Locate every blood parasite and identify its species.
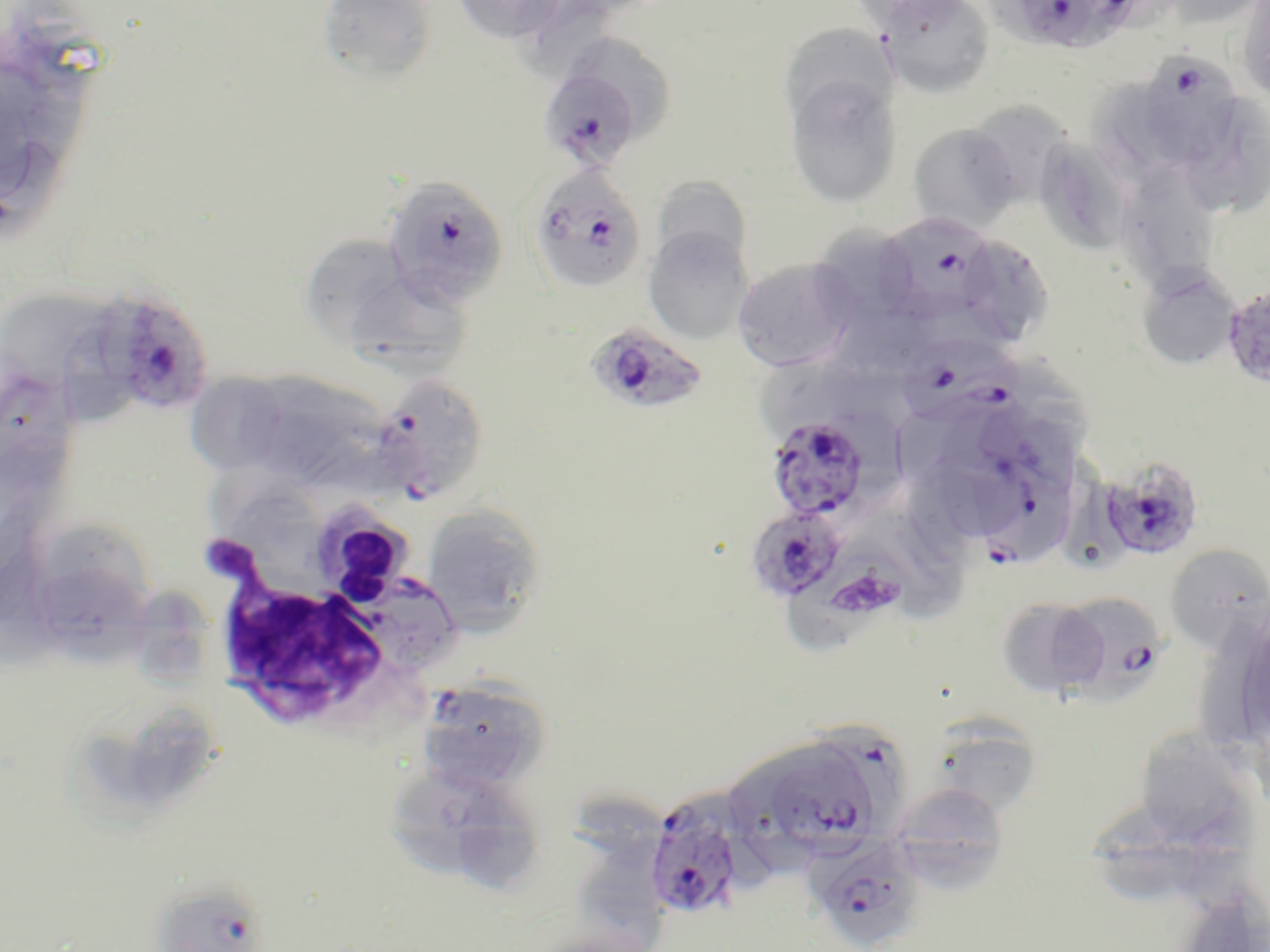
Approximate bounding boxes as (x1, y1, x2, y2) in pixels.
Plasmodium falciparum-infected red blood cells: (991, 0, 1149, 56), (1145, 53, 1235, 159), (547, 73, 633, 172), (528, 166, 647, 295), (382, 175, 507, 310), (880, 216, 995, 324), (91, 291, 214, 415), (585, 321, 710, 415), (905, 339, 1032, 430), (368, 374, 490, 503), (764, 415, 876, 522), (972, 450, 1075, 573), (1102, 455, 1205, 562), (745, 505, 847, 603), (1059, 595, 1166, 704), (417, 675, 553, 793), (817, 724, 911, 825), (775, 758, 875, 857), (644, 797, 743, 921), (807, 831, 927, 951), (151, 879, 271, 952).
No Plasmodium ovale, Plasmodium malariae, Plasmodium vivax, Babesia divergens, or Trypanosoma brucei observed.

Summary:
  - Platelet locations: (838, 577, 907, 618)
  - White blood cell locations: (215, 513, 398, 730)
  - Uninfected red blood cell locations: (317, 0, 438, 84), (451, 0, 574, 44), (849, 0, 974, 31), (1150, 0, 1268, 29), (1235, 0, 1270, 106), (525, 1, 612, 85), (877, 1, 996, 99), (789, 23, 896, 118), (574, 35, 655, 99), (618, 52, 672, 135), (784, 70, 903, 210), (1088, 78, 1176, 195), (1190, 96, 1269, 220), (983, 109, 1072, 205), (908, 123, 1021, 234), (1041, 136, 1132, 255), (650, 175, 753, 275), (1122, 190, 1216, 294), (812, 222, 914, 328), (642, 226, 754, 345), (306, 232, 407, 349), (954, 235, 1055, 348), (731, 257, 859, 371), (1136, 268, 1240, 371), (357, 282, 467, 379), (1221, 284, 1270, 390), (1, 291, 107, 375), (836, 309, 934, 379), (65, 323, 130, 433), (749, 355, 846, 436), (824, 356, 932, 437), (1000, 363, 1093, 471), (187, 370, 277, 473), (0, 375, 74, 498), (239, 376, 339, 484), (300, 385, 394, 498), (934, 457, 1020, 534), (421, 505, 547, 636), (860, 510, 973, 621), (45, 524, 151, 609), (791, 532, 902, 654), (1165, 543, 1270, 653), (33, 574, 161, 665), (140, 590, 210, 687), (997, 596, 1109, 698), (1201, 613, 1270, 753), (143, 707, 209, 797), (931, 716, 1044, 819), (1135, 719, 1249, 842), (727, 763, 821, 881), (395, 769, 492, 877), (458, 780, 547, 890), (888, 783, 1011, 891), (573, 792, 661, 861), (1089, 814, 1206, 901), (569, 844, 666, 952), (1198, 886, 1270, 952)
  - Slide-level diagnosis: Plasmodium falciparum
  - Image size: 1270×952 pixels
  - Field of view: single
  - Stain: May-Grünwald-Giemsa
  - Magnification: 1000x
  - Modality: optical microscopy
  - Preparation: thin blood film